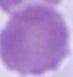

identification = erythrocyte
magnification = 1000x
modality = photomicrograph